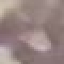
malaria_status: uninfected
image_type: cell patch, automatically extracted from a larger field of view and resized to 64 × 64 pixels
stain: Giemsa
capture: smartphone through the microscope eyepiece
preparation: thin smear